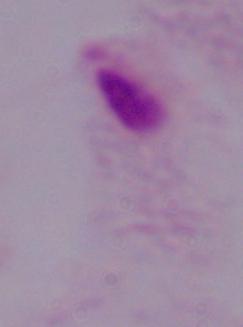

Summary:
  - Magnification: 1000x
  - Modality: photomicrograph
  - Identification: trichomonad